Classify this cell by malaria status.
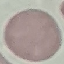

It is uninfected.

Automatically extracted cell patch, resized to 64 × 64 pixels. Acquired by smartphone through the microscope eyepiece. Giemsa stain. Thin blood film.